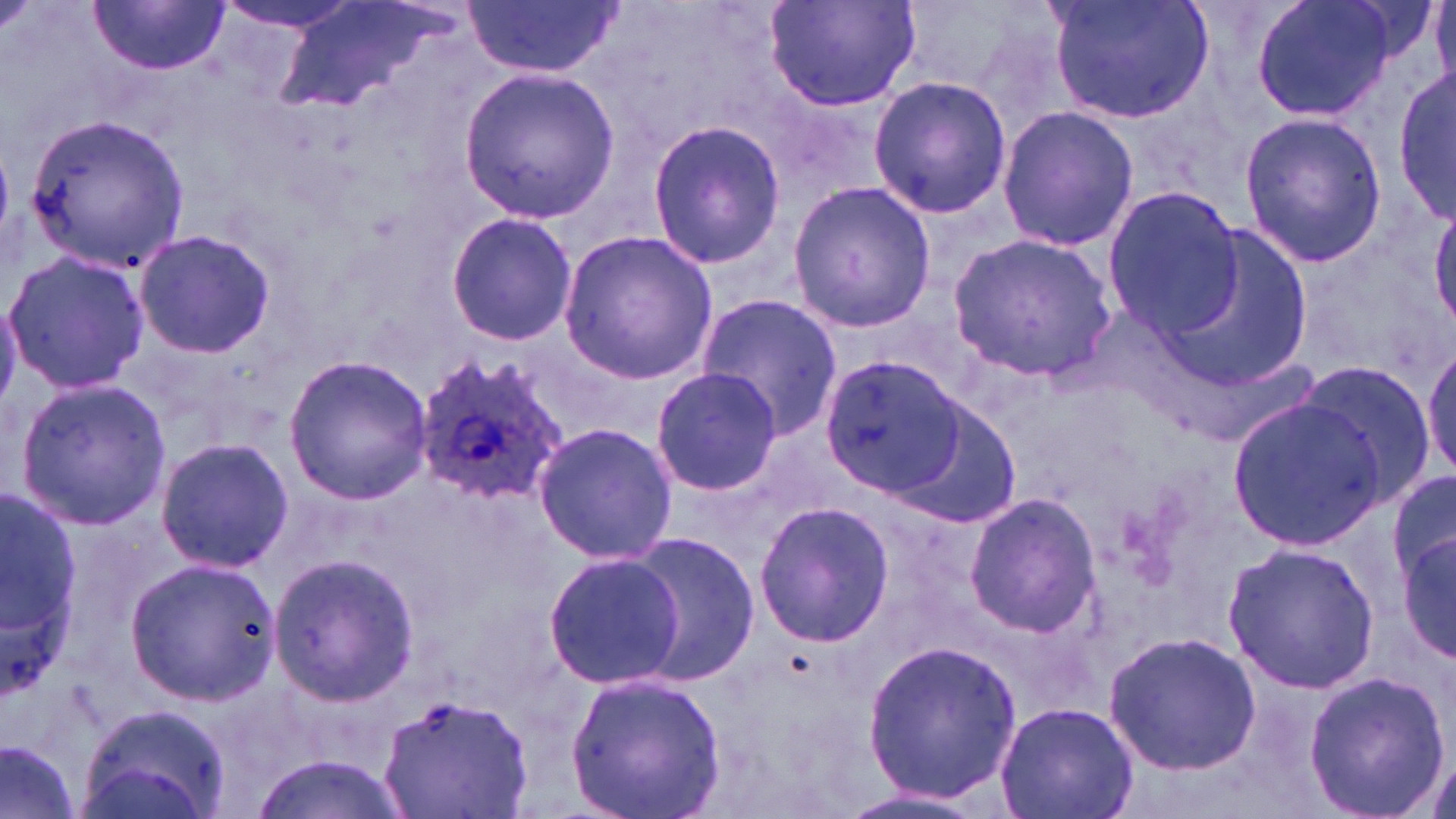

Summary:
  - Coordinate format: approximate bounding boxes as (x1, y1, x2, y2) in pixels
  - Uninfected red blood cell locations: (466, 0, 620, 78), (761, 0, 923, 114), (1048, 0, 1214, 125), (1250, 0, 1395, 124), (211, 1, 363, 35), (93, 2, 225, 76), (275, 3, 458, 121), (458, 67, 618, 222), (1395, 67, 1454, 227), (866, 75, 1012, 219), (996, 106, 1138, 251), (1240, 112, 1389, 265), (22, 115, 191, 272), (646, 119, 785, 270), (788, 181, 937, 333), (1102, 187, 1246, 337), (1430, 206, 1456, 328), (446, 210, 578, 346), (1149, 221, 1318, 398), (132, 229, 278, 359), (557, 229, 717, 384), (948, 232, 1114, 378), (3, 251, 153, 394), (696, 294, 843, 438), (1422, 341, 1456, 481), (283, 354, 432, 505), (819, 357, 965, 503), (1291, 359, 1439, 507), (650, 367, 782, 497), (14, 378, 170, 528), (890, 398, 1023, 529), (1228, 398, 1389, 550), (532, 421, 678, 565), (156, 438, 295, 573), (1388, 466, 1456, 589), (0, 488, 80, 688), (962, 492, 1103, 635), (754, 500, 894, 650), (1397, 530, 1455, 670), (622, 532, 763, 685), (1222, 543, 1382, 694), (542, 551, 684, 688), (264, 555, 415, 707), (124, 556, 278, 707), (1102, 629, 1260, 776), (862, 637, 1024, 804), (1300, 668, 1450, 819), (565, 670, 726, 819), (381, 698, 533, 818), (996, 702, 1136, 819), (80, 704, 230, 819), (0, 739, 85, 819), (250, 753, 411, 819), (835, 784, 994, 819)
  - Plasmodium ovale-infected red blood cell locations: (412, 353, 566, 505)
  - Slide-level diagnosis: Plasmodium ovale
  - Image size: 1456×819 pixels
  - Magnification: 1000x
  - Preparation: thin blood film
  - Stain: May-Grünwald-Giemsa
  - Modality: light microscopy
  - Field of view: one of a larger specimen